Classify this cell by malaria status.
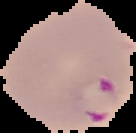

It is parasitized.

image type = segmented cell region with the area outside set to black
preparation = thin blood film
image size = 136×133 pixels